Comment on the morphology of the erythrocytes.
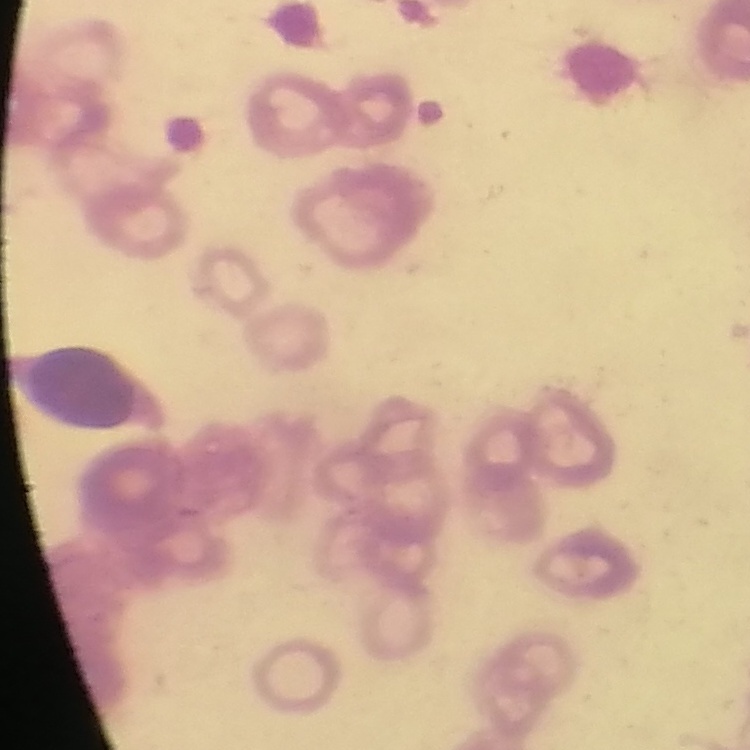

They show rouleaux formation.

image type = one tile cut from a larger photomicrograph
stain = Field's or Giemsa
preparation = thin blood film